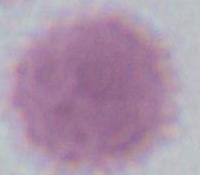
Summary:
  - Identification: erythrocyte
  - Modality: micrograph
  - Magnification: 1000x